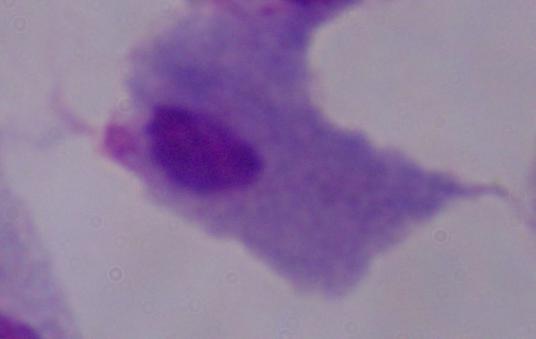
identification = trichomonad
modality = micrograph
magnification = 1000x